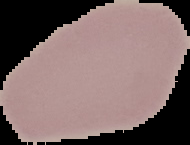
image size = 190×145 pixels
image type = segmented cell region with the area outside set to black
preparation = thin blood smear
result = no Plasmodium parasites detected